Assess the morphology of the erythrocytes.
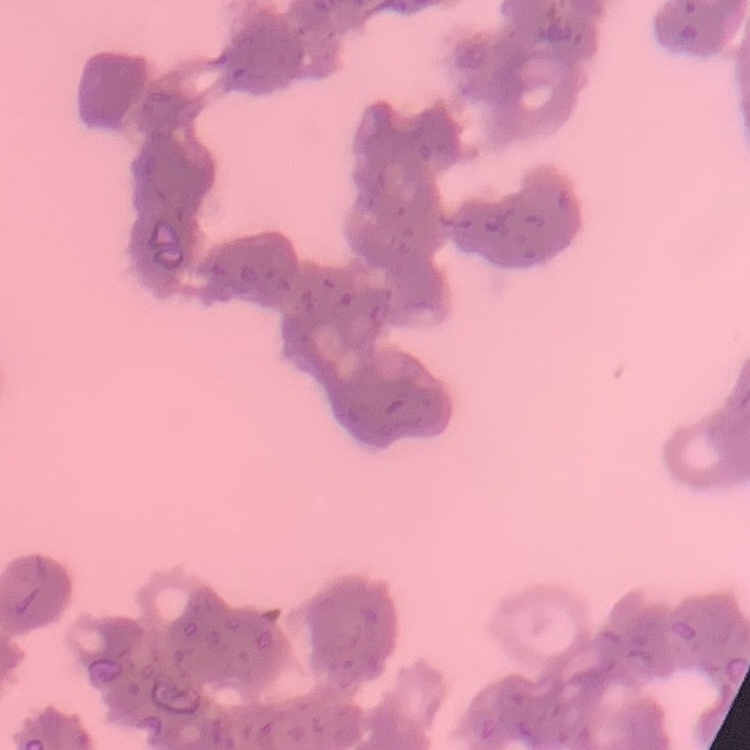
They show rouleaux formation.

image type = square crop of a larger photomicrograph
preparation = thin peripheral smear
stain = Field's or Giemsa